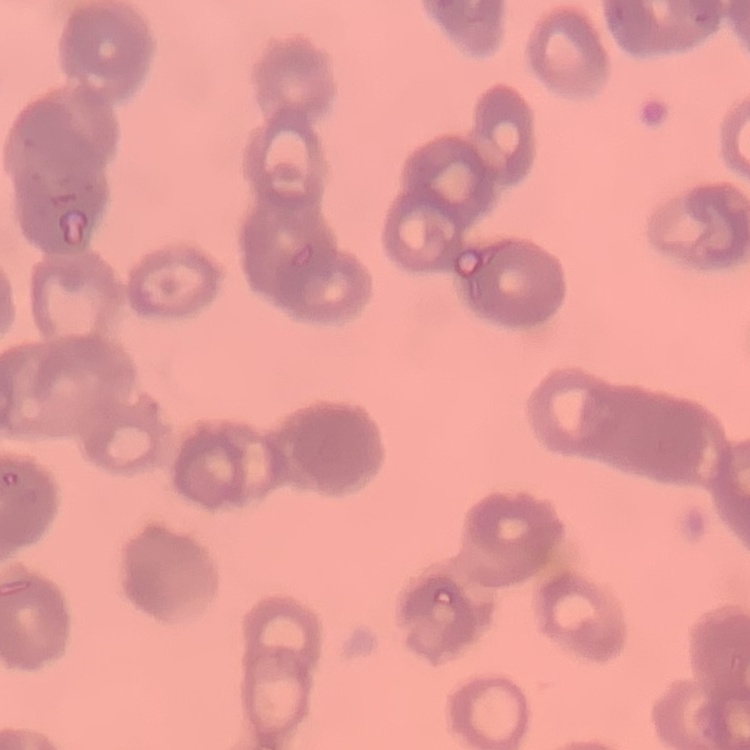
red blood cell morphology = rouleaux formation
preparation = thin blood smear
stain = Field's or Giemsa
image type = one tile cut from a larger photomicrograph